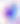

Summary:
  - Modality: micrograph
  - Identification: Toxoplasma gondii
  - Magnification: 400x